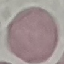
Malaria status: uninfected. Automatically extracted cell patch, resized to 64 × 64 pixels. Thin blood smear. Acquired by smartphone through the microscope eyepiece. Giemsa stain.